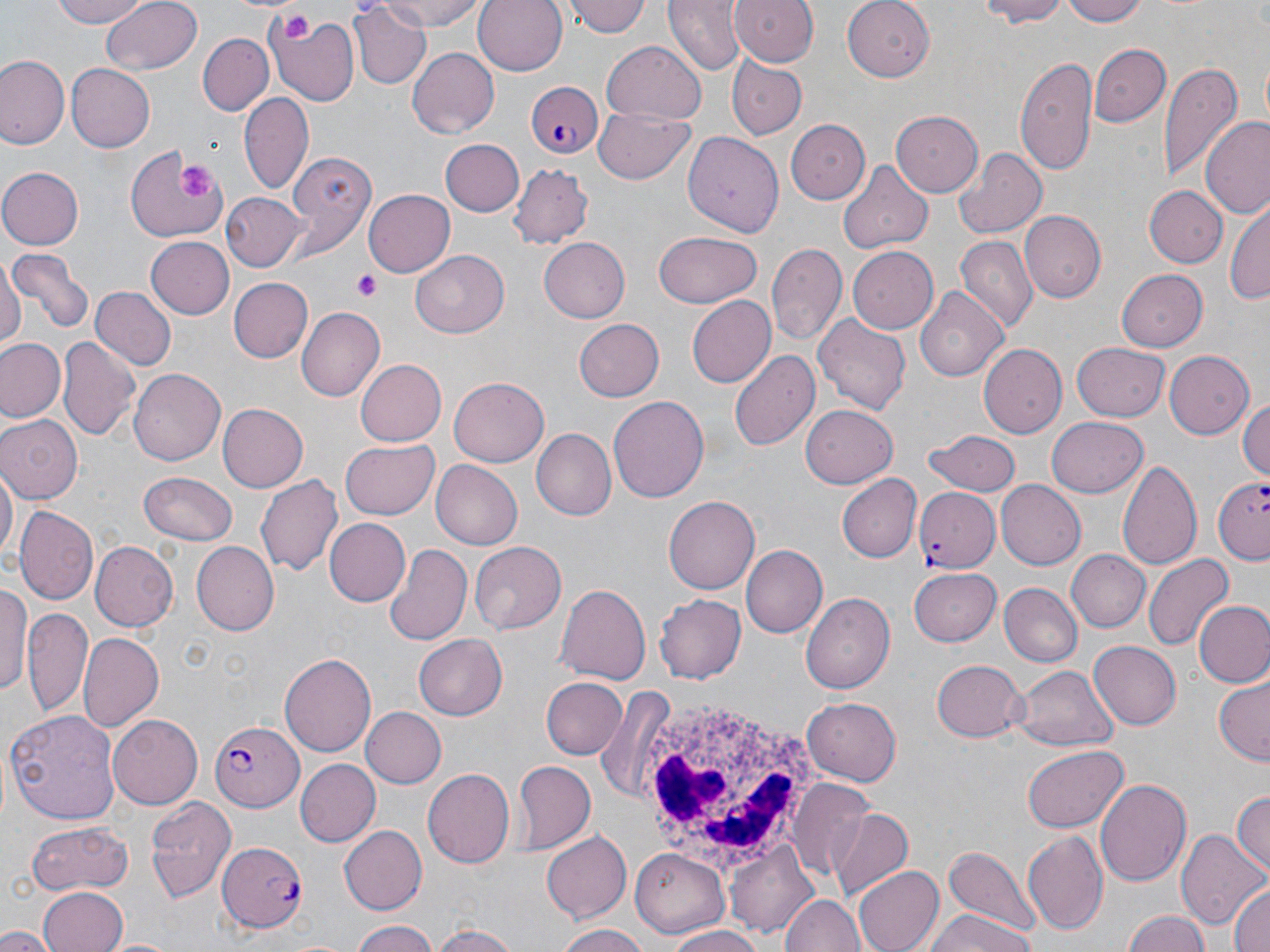
Summary:
  - Coordinate format: approximate bounding boxes as (x1,y1)-(x2,y2) corner pairs in pixels
  - White blood cell locations: (631,689)-(828,877)
  - Plasmodium falciparum-infected red blood cell locations: (524,80)-(605,161), (1211,478)-(1269,566), (916,488)-(1000,573), (210,717)-(305,809), (216,840)-(309,931)
  - Platelet locations: (281,14)-(314,43), (179,164)-(215,203), (354,271)-(382,301)
  - Uninfected red blood cell locations: (45,0)-(159,28), (101,0)-(202,75), (378,0)-(483,30), (472,0)-(567,75), (566,0)-(651,39), (664,0)-(744,76), (730,0)-(820,67), (843,0)-(938,80), (972,0)-(1075,26), (1064,0)-(1148,26), (348,2)-(432,89), (266,8)-(360,105), (198,34)-(273,114), (0,42)-(72,235), (600,42)-(708,122), (1090,43)-(1170,128), (406,46)-(498,138), (1,56)-(67,150), (1014,56)-(1097,172), (729,58)-(807,140), (1159,60)-(1242,180), (63,64)-(154,152), (239,91)-(315,192), (594,106)-(696,185), (892,111)-(983,198), (1201,116)-(1270,220), (786,120)-(871,202), (683,133)-(786,238), (440,139)-(525,217), (129,144)-(235,244), (954,149)-(1046,238), (283,150)-(376,254), (836,161)-(934,254), (508,164)-(593,247), (0,167)-(81,250), (1145,186)-(1227,266), (362,190)-(456,276), (221,193)-(305,273), (1226,200)-(1270,306), (1021,210)-(1106,301), (653,231)-(762,310), (142,235)-(233,320), (953,235)-(1034,332), (537,238)-(628,322), (768,243)-(846,350), (849,246)-(938,331), (10,249)-(91,335), (412,250)-(512,337), (0,255)-(23,352), (1117,270)-(1210,352), (229,277)-(313,362), (915,286)-(1008,380), (90,287)-(177,371), (686,295)-(774,388), (297,306)-(384,400), (813,312)-(913,417), (575,319)-(665,402), (57,336)-(138,442), (0,338)-(65,420), (1073,341)-(1171,420), (979,344)-(1067,439), (729,349)-(819,453), (1163,349)-(1255,439), (356,359)-(446,446), (129,369)-(226,466), (450,378)-(549,466), (609,396)-(709,503), (1239,396)-(1270,484), (218,403)-(307,490), (801,403)-(900,488), (0,414)-(81,503), (1044,417)-(1148,498), (531,429)-(615,520), (924,429)-(1021,498), (340,440)-(440,519), (1119,459)-(1200,574), (430,460)-(521,550), (0,467)-(16,563), (140,470)-(237,545), (255,473)-(341,580), (836,473)-(921,563), (995,480)-(1085,569), (664,494)-(761,594), (15,504)-(97,605), (327,517)-(411,607), (470,541)-(565,632), (89,542)-(178,631), (190,542)-(277,634), (384,542)-(474,648), (741,545)-(826,640), (1068,549)-(1149,632), (1145,552)-(1232,651), (909,567)-(1001,646), (0,582)-(31,701), (554,582)-(649,683), (998,583)-(1082,668), (802,592)-(895,695), (654,593)-(747,683), (1194,599)-(1270,688), (22,610)-(94,718), (77,631)-(163,730), (415,633)-(507,720), (1087,642)-(1181,730), (279,651)-(376,760), (931,660)-(1026,742), (1012,665)-(1116,751), (1213,676)-(1269,764), (541,677)-(624,760), (596,690)-(676,802), (804,699)-(900,785), (361,707)-(445,789), (5,709)-(121,823), (106,715)-(202,809), (1021,745)-(1128,834), (295,759)-(381,847), (511,762)-(595,852), (422,769)-(514,871), (1096,778)-(1195,888), (789,783)-(878,882), (1231,789)-(1269,880), (144,796)-(235,905), (824,805)-(912,895), (25,818)-(136,895), (340,825)-(426,912), (1021,827)-(1108,935), (1178,828)-(1267,936), (541,831)-(633,923), (727,840)-(818,935), (940,844)-(1041,939), (631,849)-(729,939), (852,865)-(943,952), (1227,881)-(1270,952), (39,887)-(130,952), (781,894)-(863,952), (922,910)-(1040,952), (1123,910)-(1209,952), (350,919)-(440,952), (427,921)-(520,952), (554,923)-(650,952), (662,926)-(767,952), (0,927)-(54,952)
  - Slide-level diagnosis: Plasmodium falciparum
  - Modality: optical microscopy
  - Preparation: thin blood film
  - Magnification: 1000x
  - Field of view: single
  - Image size: 1270×952 pixels
  - Stain: May-Grünwald-Giemsa